Give the position of every Plasmodium parasite.
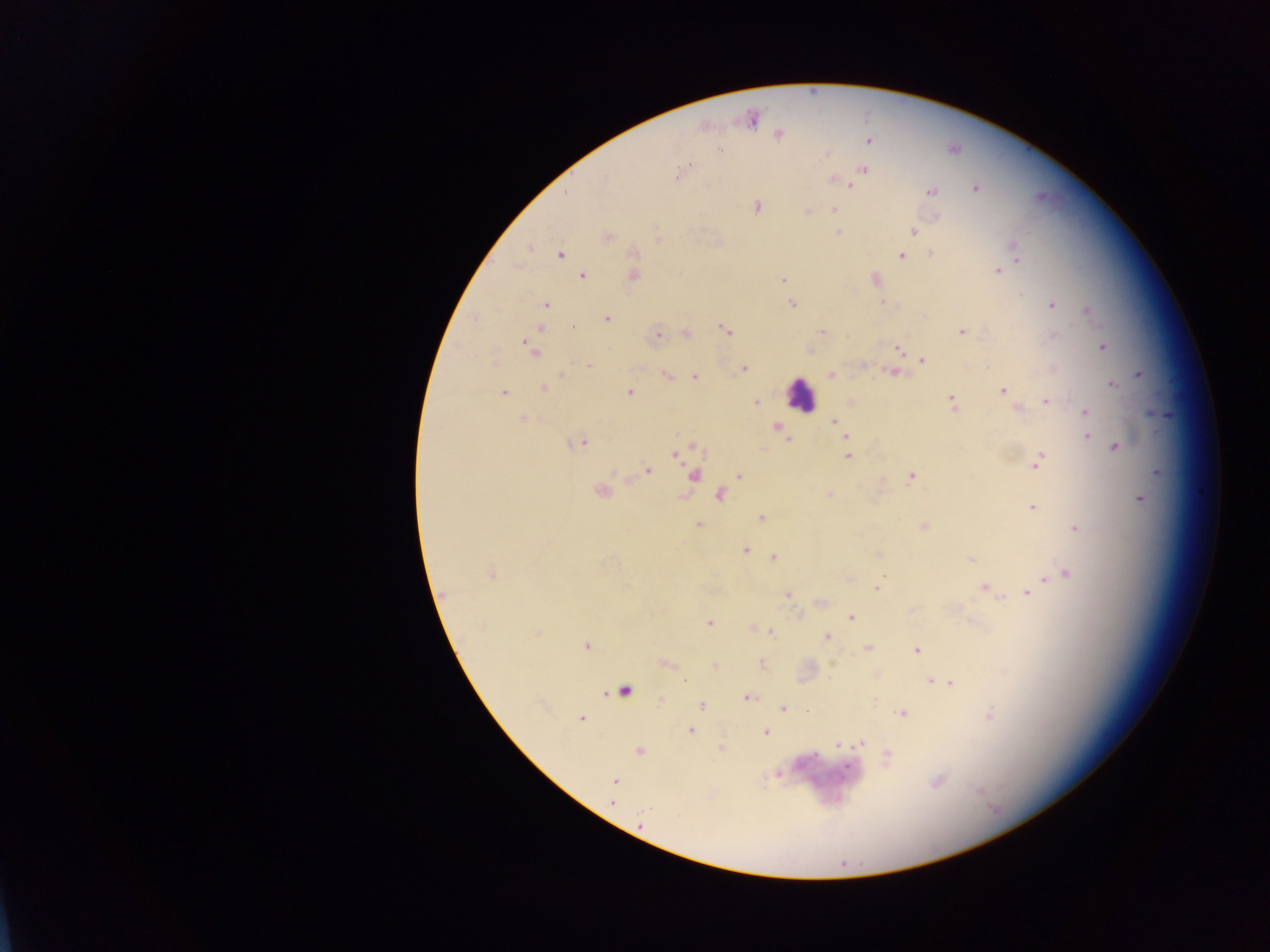
Approximate centers as (x, y) in pixels.
Plasmodium parasites: (751, 118), (705, 127), (778, 134), (869, 141), (719, 150), (863, 170), (682, 171), (833, 179), (851, 184), (975, 188), (932, 191), (757, 207), (835, 209), (808, 211), (938, 216), (913, 231), (838, 232), (607, 237), (658, 240), (529, 248), (1014, 249), (559, 254), (931, 255), (901, 256), (1016, 258), (998, 271), (583, 276), (634, 276), (875, 279), (783, 280), (883, 303), (791, 304), (545, 305), (1052, 305), (1087, 311), (606, 318), (541, 328), (573, 328), (725, 330), (821, 332), (961, 332), (686, 334), (658, 335), (1102, 347), (531, 349), (899, 350), (923, 360), (589, 366), (744, 369), (893, 373), (666, 374), (832, 374), (1140, 374), (695, 376), (1111, 385), (543, 388), (1002, 390), (504, 393), (630, 393), (952, 401), (1046, 401), (755, 402), (1017, 409), (1086, 412), (523, 419), (834, 421), (776, 427), (840, 431), (784, 434), (1087, 436), (845, 437), (789, 438), (580, 443), (1116, 447), (676, 453), (847, 456), (1038, 460), (648, 469), (693, 475), (739, 476), (911, 477), (601, 491), (830, 494), (720, 496), (1140, 499), (1032, 508), (761, 517), (699, 525), (923, 527), (1075, 528), (745, 550), (877, 555), (773, 557), (971, 559), (491, 573), (1066, 574), (1045, 581), (984, 588), (877, 589), (1027, 592), (444, 594), (787, 595), (821, 602), (851, 617), (710, 622), (761, 629), (770, 632), (536, 634), (827, 637), (586, 645), (868, 648), (917, 650), (762, 663), (665, 664), (715, 667), (685, 680), (932, 681), (945, 683), (624, 690), (747, 698), (875, 700), (660, 701), (702, 706), (783, 708), (808, 711), (903, 713), (581, 718), (690, 730), (765, 732), (861, 744), (839, 745), (721, 749), (639, 751), (887, 755), (847, 767), (614, 780), (612, 802).

Leukocyte locations: (801, 394). Single field of view. Image is 1270×952 pixels. Sample from Ghana. Photographed through a microscope with a mobile-phone camera. Thick blood film.